Locate every leukocyte (white blood cell).
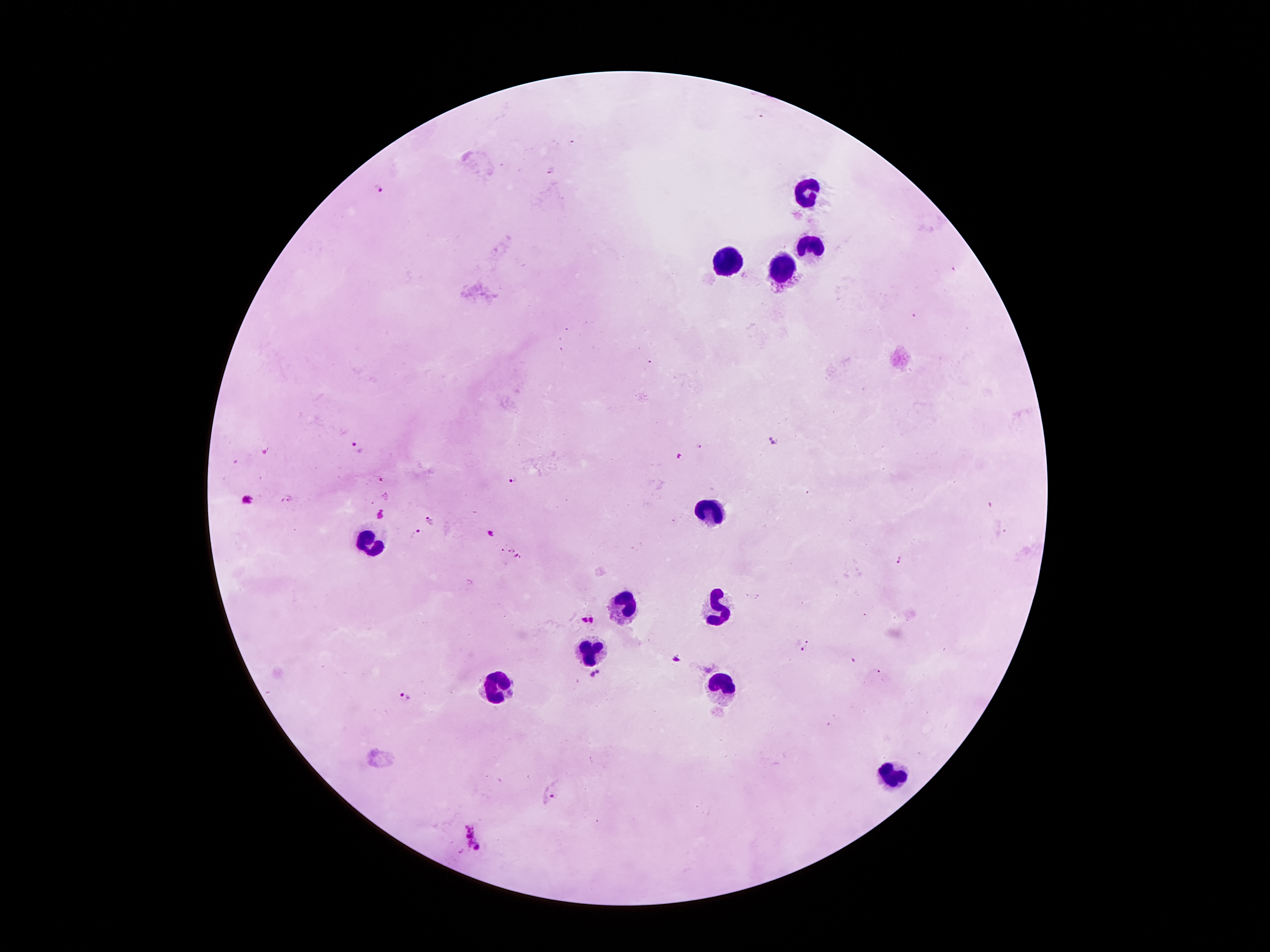

Approximate centers as [x, y] in pixels.
Leukocytes: [804, 191], [813, 246], [729, 262], [783, 271], [715, 511], [370, 536], [627, 604], [718, 607], [590, 645], [495, 684], [722, 684], [888, 775].

Malaria parasite locations: [379, 188], [774, 440], [357, 448], [264, 449], [678, 456], [513, 480], [247, 499], [382, 515], [431, 521], [416, 533], [490, 534], [501, 548], [511, 552], [517, 557], [584, 620], [592, 620], [806, 647], [675, 658], [706, 668], [598, 672], [592, 674], [403, 696], [548, 797], [474, 835]. Patient malaria status: positive for Plasmodium falciparum. Giemsa-stained preparation. Thick blood film. Photographed through the microscope eyepiece with a smartphone camera. 100x magnification. Image is 1270×952 pixels. One field from this slide.